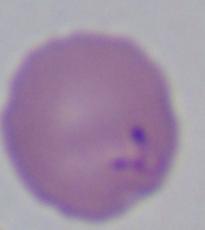

modality = micrograph
identification = Babesia
magnification = 1000x